Look for Plasmodium parasites.
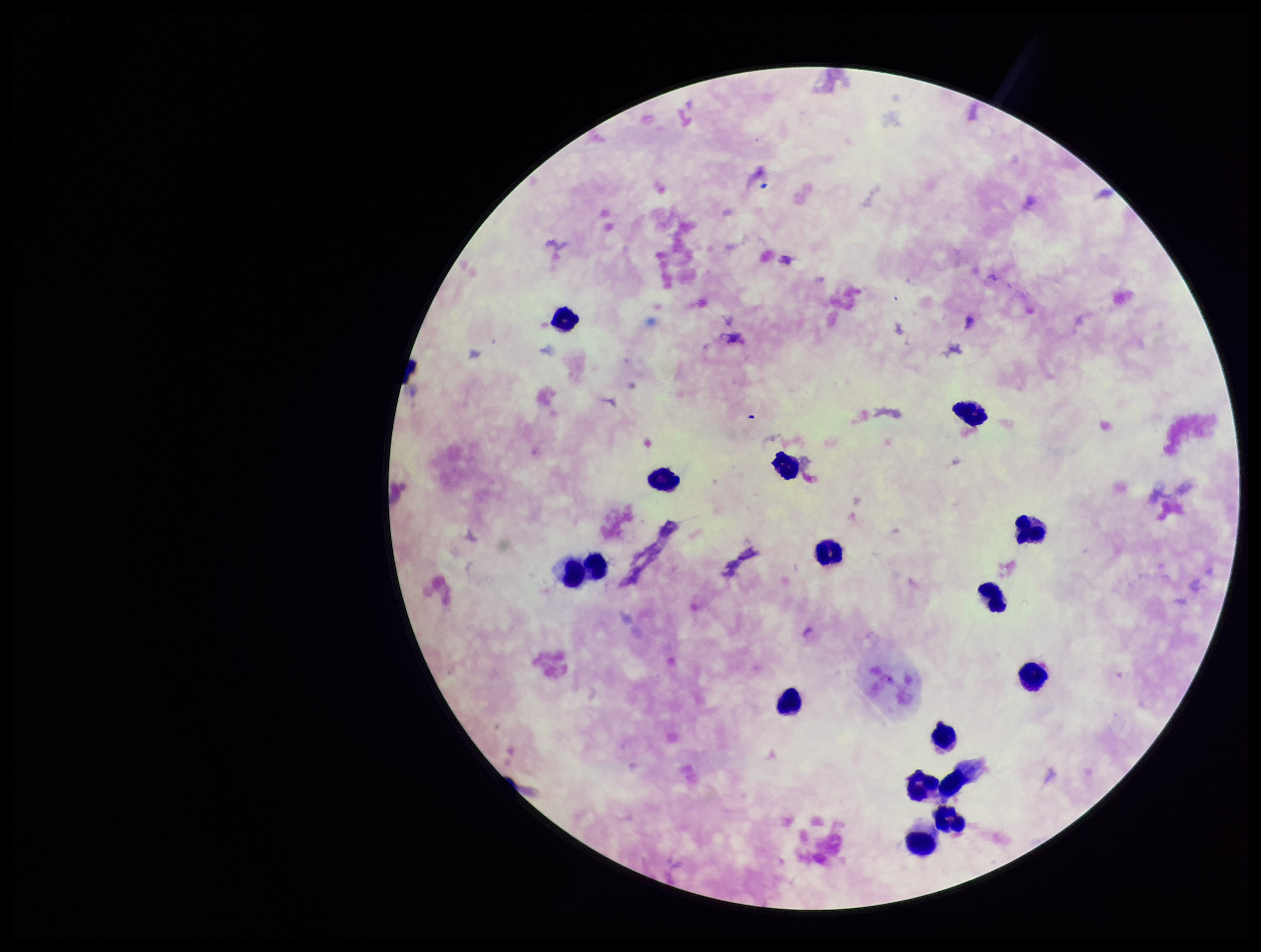

None detected.

stain = Giemsa
field of view = one from this slide
capture = smartphone photograph through the microscope eyepiece
patient malaria status = infected
species reported for this patient = Plasmodium falciparum
parasite count = 0
preparation = thick
image size = 1261×952 pixels
leukocyte count = 16